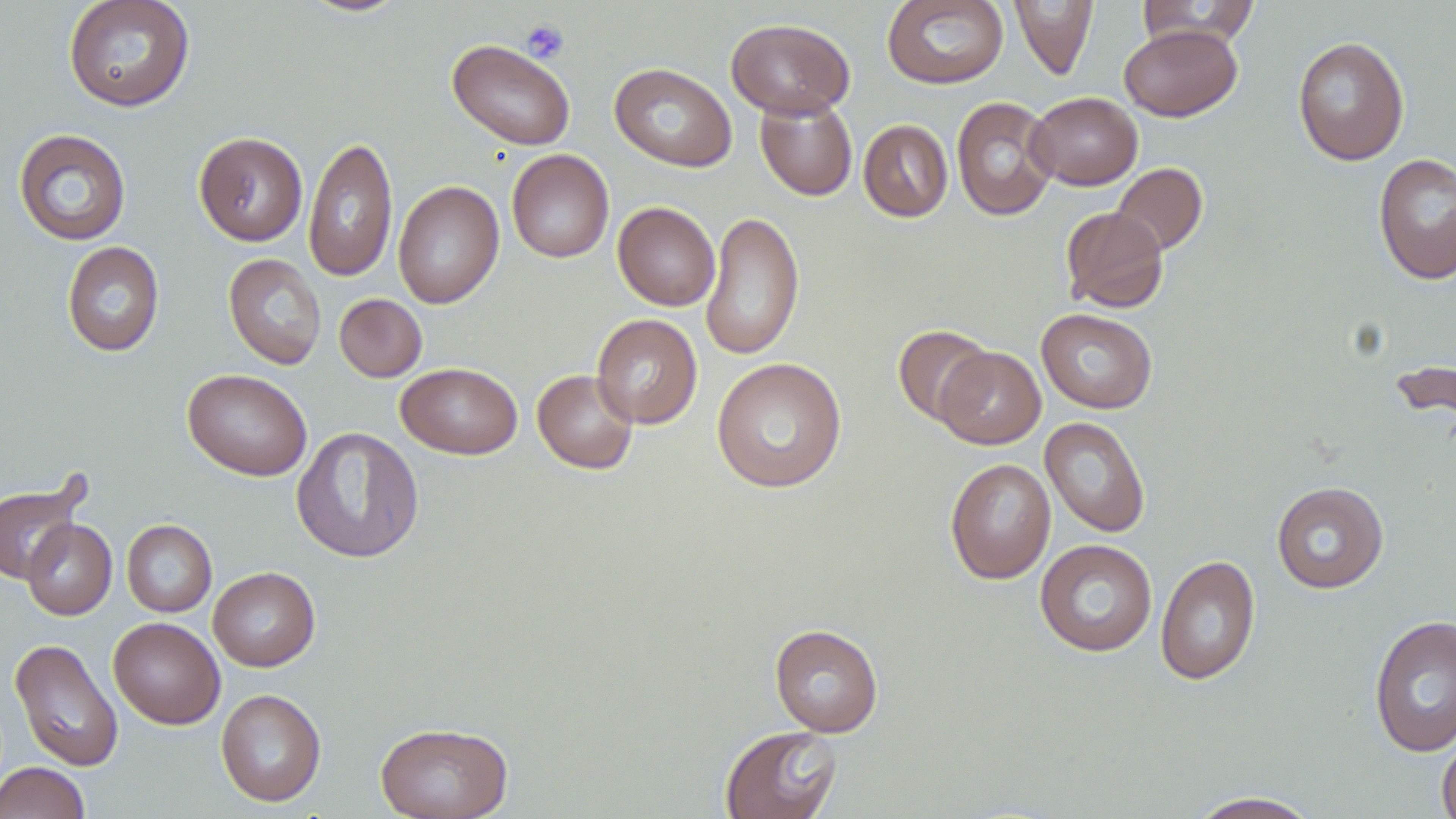

Summary:
  - Coordinate format: approximate bounding boxes as named x1/y1/x2/y2 corners in pixels
  - Uninfected red blood cell locations: (x1=62, y1=0, x2=196, y2=113), (x1=296, y1=0, x2=414, y2=18), (x1=881, y1=0, x2=1009, y2=90), (x1=1008, y1=0, x2=1098, y2=80), (x1=1134, y1=0, x2=1261, y2=48), (x1=726, y1=18, x2=856, y2=119), (x1=1119, y1=24, x2=1242, y2=121), (x1=1292, y1=36, x2=1410, y2=165), (x1=447, y1=39, x2=576, y2=151), (x1=609, y1=62, x2=737, y2=172), (x1=1027, y1=92, x2=1142, y2=190), (x1=755, y1=96, x2=857, y2=201), (x1=951, y1=96, x2=1059, y2=221), (x1=858, y1=119, x2=953, y2=222), (x1=13, y1=128, x2=132, y2=246), (x1=194, y1=131, x2=308, y2=246), (x1=304, y1=135, x2=398, y2=283), (x1=507, y1=149, x2=614, y2=263), (x1=1373, y1=152, x2=1456, y2=286), (x1=1111, y1=162, x2=1208, y2=256), (x1=392, y1=180, x2=504, y2=309), (x1=612, y1=202, x2=720, y2=311), (x1=1060, y1=206, x2=1169, y2=313), (x1=700, y1=210, x2=805, y2=361), (x1=62, y1=241, x2=164, y2=356), (x1=223, y1=252, x2=326, y2=370), (x1=334, y1=294, x2=427, y2=382), (x1=1036, y1=308, x2=1158, y2=414), (x1=591, y1=314, x2=703, y2=429), (x1=892, y1=324, x2=994, y2=426), (x1=935, y1=346, x2=1046, y2=449), (x1=711, y1=357, x2=848, y2=493), (x1=396, y1=362, x2=523, y2=460), (x1=182, y1=368, x2=312, y2=481), (x1=532, y1=369, x2=639, y2=474), (x1=1040, y1=416, x2=1151, y2=538), (x1=291, y1=426, x2=424, y2=564), (x1=944, y1=457, x2=1056, y2=584), (x1=0, y1=478, x2=85, y2=583), (x1=1271, y1=481, x2=1389, y2=594), (x1=21, y1=519, x2=117, y2=620), (x1=122, y1=519, x2=217, y2=617), (x1=1034, y1=539, x2=1158, y2=657), (x1=1155, y1=554, x2=1260, y2=686), (x1=208, y1=566, x2=320, y2=671), (x1=1368, y1=613, x2=1456, y2=758), (x1=108, y1=616, x2=225, y2=729), (x1=769, y1=624, x2=884, y2=737), (x1=10, y1=639, x2=123, y2=772), (x1=215, y1=688, x2=326, y2=807), (x1=375, y1=722, x2=513, y2=818), (x1=720, y1=725, x2=842, y2=819), (x1=1436, y1=732, x2=1456, y2=819), (x1=0, y1=762, x2=90, y2=819), (x1=1185, y1=791, x2=1324, y2=818)
  - Platelet locations: (x1=521, y1=20, x2=569, y2=64)
  - Slide-level diagnosis: negative for blood parasites
  - Magnification: 1000x
  - Stain: May-Grünwald-Giemsa
  - Preparation: thin blood smear
  - Image size: 1456×819 pixels
  - Field of view: one of a larger specimen
  - Modality: optical microscopy